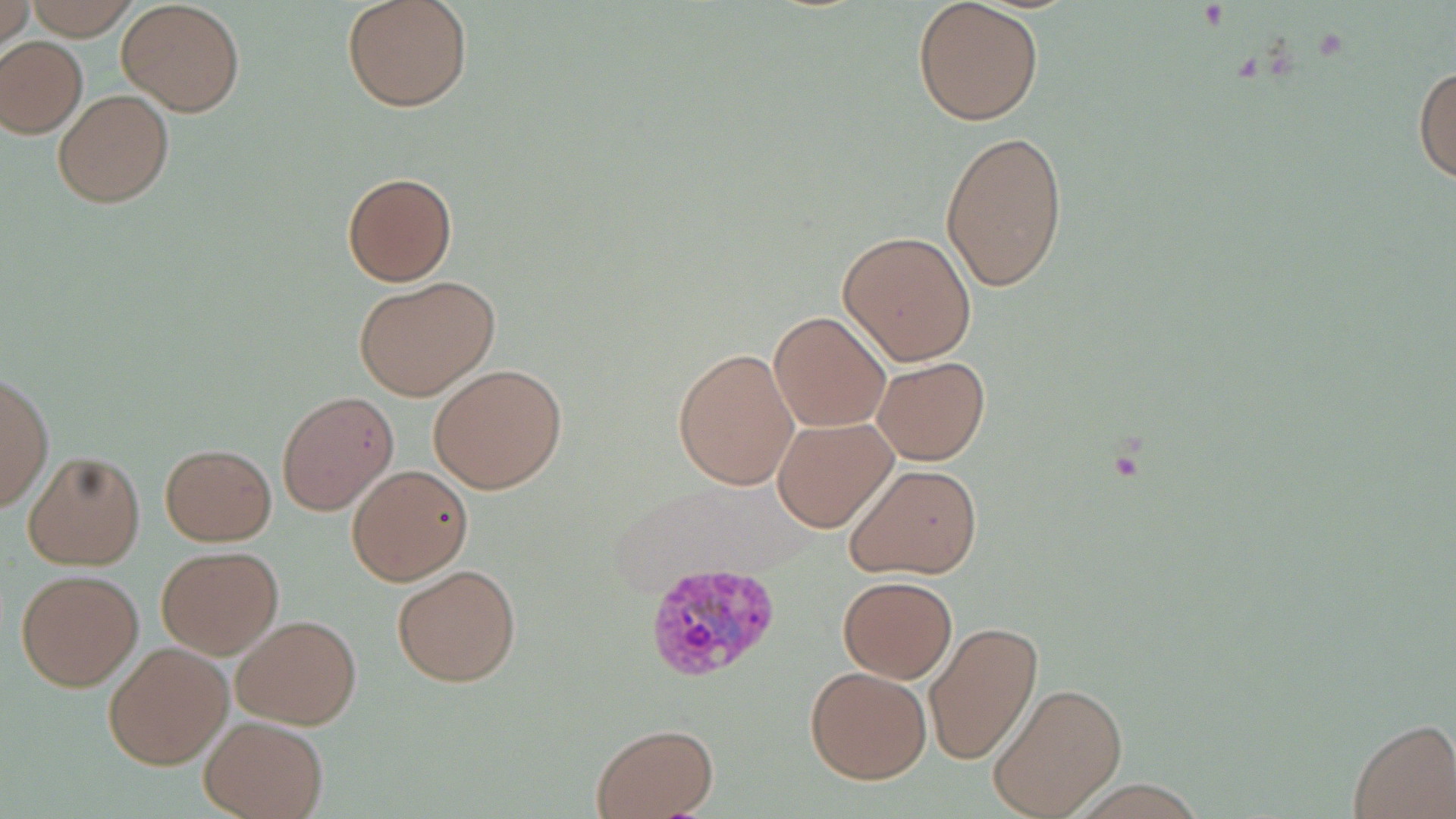

Approximate bounding boxes as (x1, y1, x2, y2) in pixels. Plasmodium vivax-infected red blood cell locations: (645, 561, 784, 681). Uninfected red blood cell locations: (1, 0, 31, 52), (22, 0, 144, 40), (342, 0, 473, 112), (116, 1, 246, 117), (912, 1, 1044, 125), (0, 36, 87, 138), (1413, 61, 1456, 188), (53, 88, 174, 208), (940, 128, 1068, 292), (343, 172, 457, 286), (837, 230, 977, 364), (354, 275, 499, 401), (812, 275, 972, 413), (769, 310, 891, 431), (672, 347, 799, 491), (872, 356, 989, 464), (427, 363, 567, 494), (0, 372, 52, 514), (275, 390, 399, 516), (771, 415, 897, 533), (159, 442, 277, 546), (22, 449, 145, 570), (844, 463, 980, 578), (346, 464, 472, 586), (156, 544, 283, 659), (392, 564, 522, 687), (15, 567, 143, 692), (837, 575, 956, 682), (231, 612, 362, 729), (925, 621, 1042, 767), (104, 641, 232, 769), (804, 664, 932, 784), (986, 680, 1129, 819), (199, 715, 327, 819), (1348, 719, 1455, 817), (589, 723, 719, 818). Slide-level diagnosis: Plasmodium vivax. Captured at 1000x magnification. Thin blood smear. Image is 1456×819 pixels. Single field of view. Light microscopy. May-Grünwald-Giemsa stain.